Locate every Plasmodium falciparum-infected red blood cell.
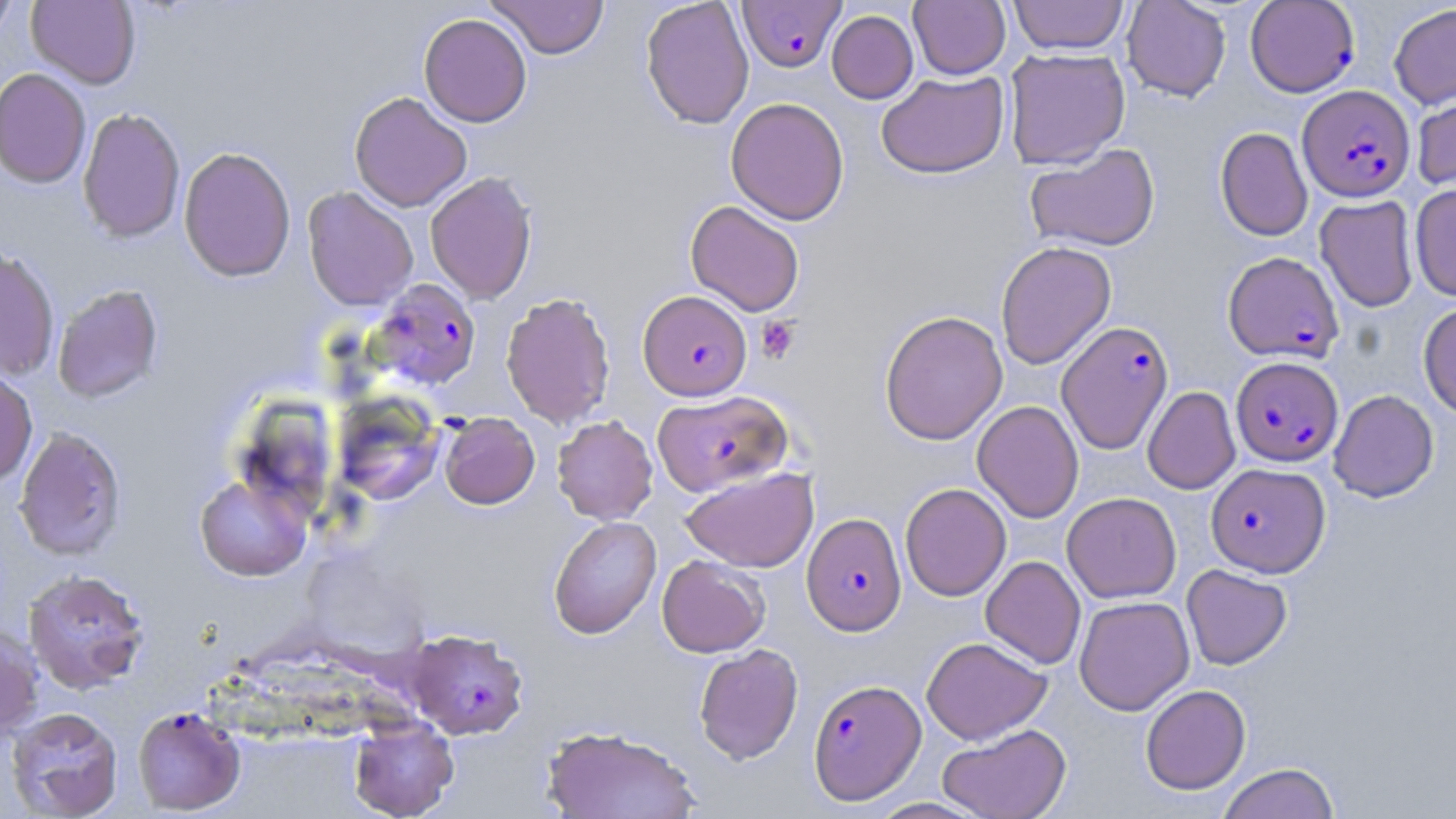

Approximate bounding boxes as [x1, y1, x2, y2] in pixels.
Plasmodium falciparum-infected red blood cells: [738, 1, 846, 72], [1246, 1, 1359, 97], [1298, 84, 1415, 202], [1223, 251, 1343, 363], [369, 278, 482, 391], [638, 290, 752, 400], [1056, 320, 1174, 454], [1231, 356, 1343, 467], [652, 389, 793, 496], [1206, 462, 1330, 577], [802, 512, 906, 635], [405, 629, 528, 740], [808, 678, 926, 804], [132, 706, 245, 815].

Summary:
  - Platelet locations: [756, 316, 801, 363]
  - Uninfected red blood cell locations: [26, 0, 141, 89], [486, 0, 610, 59], [640, 0, 754, 129], [909, 0, 1010, 79], [1009, 0, 1128, 54], [1121, 0, 1231, 102], [0, 1, 19, 45], [1389, 3, 1456, 109], [826, 10, 918, 104], [418, 13, 532, 127], [1004, 48, 1130, 169], [0, 68, 92, 189], [876, 71, 1009, 178], [1412, 83, 1456, 194], [349, 91, 472, 212], [726, 97, 850, 225], [77, 107, 186, 244], [1215, 127, 1312, 242], [1024, 144, 1160, 252], [178, 146, 296, 282], [425, 171, 537, 304], [1410, 185, 1456, 301], [302, 187, 418, 311], [1315, 195, 1419, 312], [685, 200, 805, 316], [995, 241, 1116, 369], [0, 248, 60, 381], [52, 284, 164, 403], [501, 292, 616, 429], [1418, 302, 1456, 418], [879, 310, 1008, 445], [0, 368, 38, 489], [1143, 386, 1240, 494], [1328, 390, 1439, 502], [333, 394, 445, 506], [972, 400, 1084, 523], [439, 412, 540, 509], [552, 415, 658, 525], [14, 426, 127, 561], [681, 467, 818, 573], [195, 471, 313, 582], [900, 482, 1011, 601], [1062, 492, 1181, 603], [548, 516, 662, 639], [657, 554, 770, 657], [981, 556, 1086, 669], [1181, 564, 1292, 670], [23, 569, 150, 694], [1074, 596, 1195, 715], [0, 625, 44, 740], [921, 636, 1051, 744], [694, 643, 804, 764], [1140, 684, 1251, 795], [5, 706, 123, 818], [348, 716, 458, 819], [937, 723, 1071, 819], [542, 725, 699, 819], [1217, 763, 1341, 819], [867, 797, 990, 818]
  - Slide-level diagnosis: Plasmodium falciparum
  - Preparation: thin blood film
  - Stain: May-Grünwald-Giemsa
  - Field of view: single
  - Magnification: 1000x
  - Modality: light microscopy
  - Image size: 1456×819 pixels